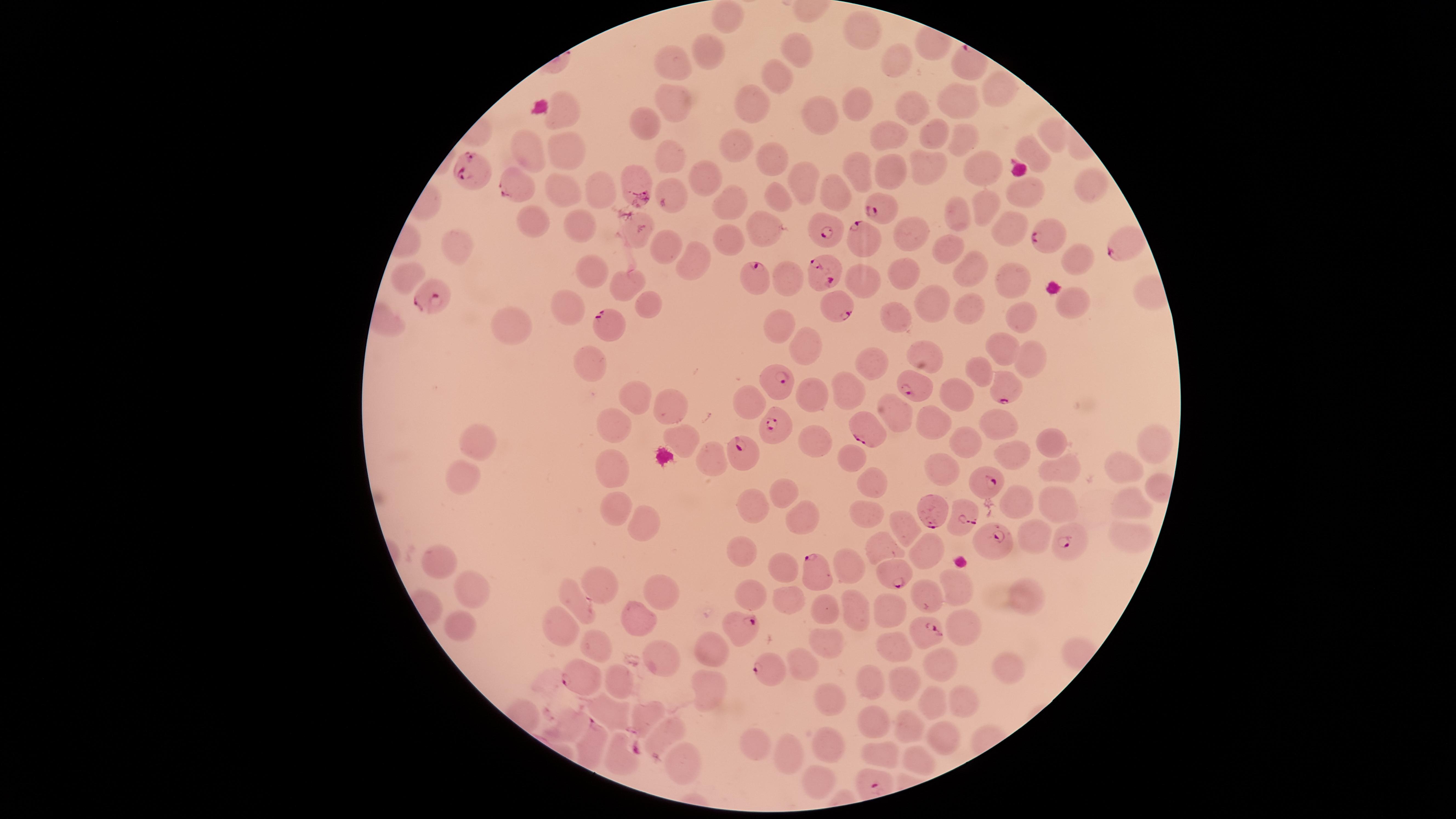

Approximate marker points as [x, y] in pixels. Uninfected red blood cells: [731, 15], [861, 25], [799, 47], [706, 48], [673, 57], [899, 59], [773, 72], [1002, 88], [753, 102], [673, 103], [911, 104], [856, 105], [961, 105], [820, 114], [566, 115], [644, 119], [1054, 127], [929, 129], [894, 132], [958, 135], [734, 149], [1030, 149], [528, 152], [564, 154], [667, 155], [921, 159], [768, 161], [887, 166], [984, 168], [857, 169], [701, 174], [801, 180], [636, 181], [1087, 183], [555, 188], [594, 190], [834, 193], [670, 194], [1027, 196], [773, 197], [729, 200], [988, 203], [962, 212], [577, 224], [1010, 224], [538, 225], [636, 229], [759, 229], [910, 229], [727, 235], [456, 247], [660, 248], [945, 251], [1077, 254], [694, 259], [585, 267], [972, 268], [863, 273], [902, 273], [407, 276], [785, 277], [1018, 280], [626, 283], [646, 301], [938, 301], [567, 302], [1071, 302], [968, 308], [1023, 315], [898, 317], [785, 324], [513, 328], [808, 347], [1001, 347], [929, 354], [1028, 360], [584, 363], [872, 364], [986, 368], [844, 388], [957, 388], [747, 394], [811, 395], [633, 396], [667, 402], [900, 416], [933, 419], [999, 420], [616, 424], [970, 439], [679, 440], [817, 441], [1044, 443], [1153, 443], [481, 446], [1012, 452], [708, 455], [849, 457], [938, 463], [1120, 468], [1060, 470], [613, 472], [875, 481], [463, 484], [785, 488], [1015, 500], [1053, 500], [755, 503], [1123, 503], [609, 508], [638, 511], [866, 513], [810, 518], [904, 529], [1032, 533], [1124, 540], [923, 545], [882, 546], [743, 549], [439, 561], [853, 567], [783, 574], [472, 582], [750, 585], [956, 585], [668, 587], [603, 589], [1025, 597], [577, 600], [789, 600], [862, 605], [827, 609], [889, 609], [642, 618], [560, 625], [459, 626], [965, 626], [829, 640], [590, 647], [717, 647], [898, 647], [664, 654], [808, 663], [939, 665], [1004, 666], [876, 681], [904, 681], [625, 686], [713, 689], [962, 696], [834, 697], [932, 700], [649, 711], [618, 715], [569, 724], [875, 727], [916, 728], [670, 731], [944, 734], [755, 741], [830, 745], [881, 751], [788, 754], [618, 755], [922, 755], [684, 766], [821, 782]. Parasitized red blood cells: [470, 169], [509, 185], [881, 208], [824, 229], [862, 238], [1045, 239], [1115, 249], [822, 271], [755, 276], [431, 294], [837, 307], [609, 320], [781, 384], [918, 384], [1008, 393], [775, 427], [866, 429], [742, 455], [990, 483], [929, 510], [964, 516], [1069, 541], [994, 543], [818, 570], [892, 576], [735, 625], [925, 633], [769, 667], [578, 679], [591, 742]. Species: Plasmodium falciparum. Thin smear of blood. Smartphone photograph through the microscope eyepiece. Single field of view. Presence: malaria parasites identified. Giemsa-stained preparation. Circular visible region. Image is 1456×819 pixels.